Outline each blood parasite and name the species.
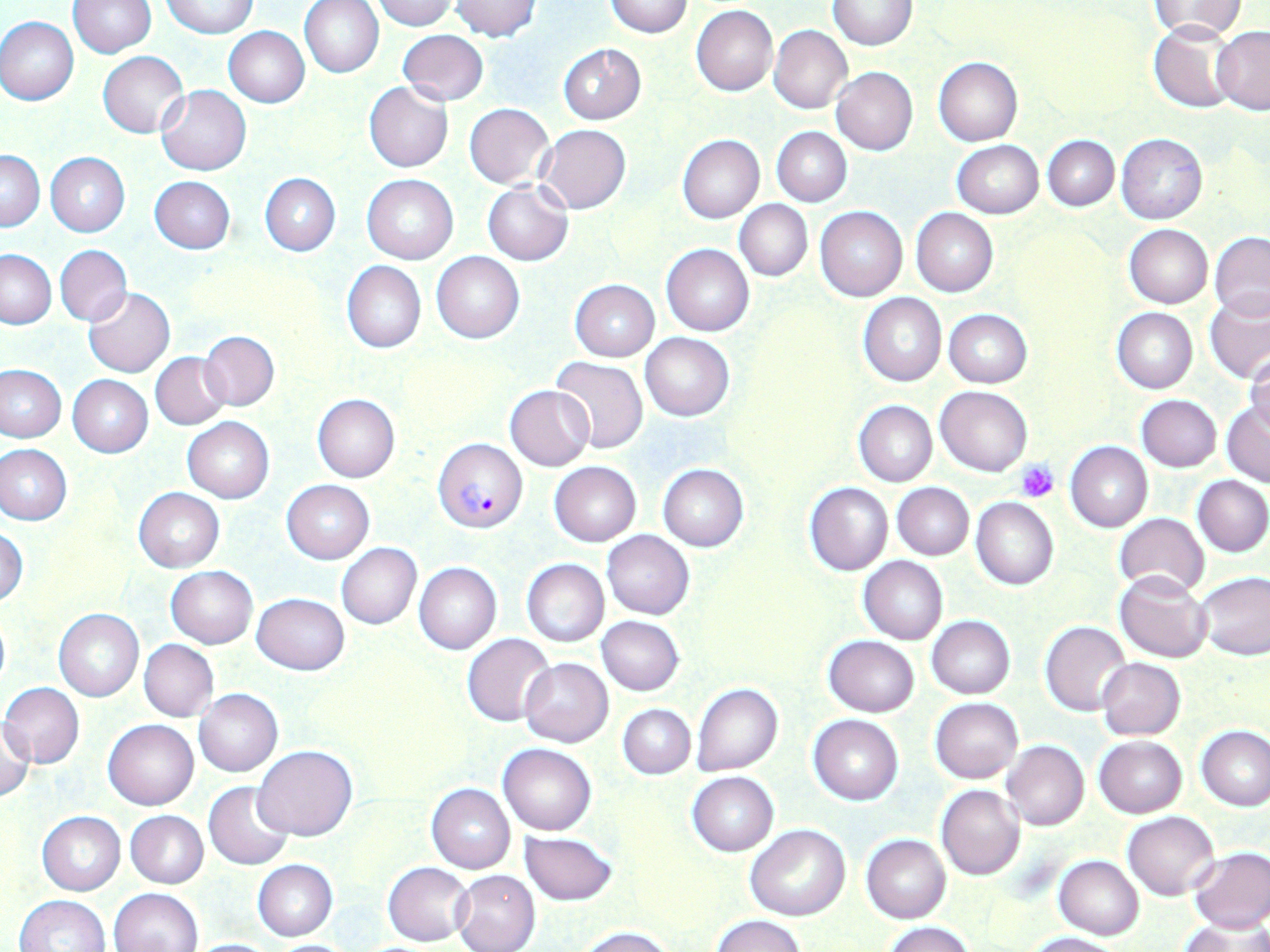
Approximate bounding boxes as named x1/y1/x2/y2 corners in pixels.
Plasmodium falciparum-infected red blood cells: (x1=434, y1=437, x2=527, y2=532).
No Plasmodium ovale, Plasmodium malariae, Plasmodium vivax, Babesia divergens, or Trypanosoma brucei observed.

Platelet locations: (x1=1014, y1=460, x2=1059, y2=502). Uninfected red blood cell locations: (x1=68, y1=0, x2=157, y2=58), (x1=299, y1=0, x2=385, y2=78), (x1=373, y1=0, x2=457, y2=30), (x1=448, y1=0, x2=542, y2=43), (x1=827, y1=0, x2=918, y2=50), (x1=1151, y1=0, x2=1249, y2=42), (x1=160, y1=1, x2=258, y2=37), (x1=605, y1=1, x2=693, y2=38), (x1=691, y1=5, x2=778, y2=96), (x1=1, y1=16, x2=79, y2=105), (x1=1148, y1=23, x2=1240, y2=112), (x1=769, y1=24, x2=852, y2=114), (x1=223, y1=26, x2=309, y2=107), (x1=1210, y1=26, x2=1270, y2=114), (x1=396, y1=30, x2=488, y2=106), (x1=558, y1=44, x2=647, y2=124), (x1=98, y1=52, x2=188, y2=137), (x1=933, y1=57, x2=1022, y2=145), (x1=831, y1=67, x2=918, y2=155), (x1=364, y1=82, x2=454, y2=172), (x1=157, y1=85, x2=250, y2=176), (x1=464, y1=103, x2=554, y2=189), (x1=536, y1=124, x2=631, y2=214), (x1=773, y1=127, x2=851, y2=206), (x1=1116, y1=133, x2=1208, y2=225), (x1=677, y1=134, x2=764, y2=223), (x1=1043, y1=135, x2=1119, y2=211), (x1=951, y1=141, x2=1042, y2=218), (x1=1, y1=149, x2=43, y2=231), (x1=46, y1=152, x2=130, y2=237), (x1=260, y1=173, x2=340, y2=255), (x1=361, y1=174, x2=457, y2=263), (x1=149, y1=176, x2=236, y2=254), (x1=483, y1=180, x2=573, y2=265), (x1=735, y1=201, x2=813, y2=281), (x1=815, y1=206, x2=907, y2=302), (x1=911, y1=207, x2=998, y2=296), (x1=1124, y1=224, x2=1213, y2=308), (x1=1210, y1=231, x2=1270, y2=320), (x1=54, y1=244, x2=132, y2=327), (x1=662, y1=244, x2=754, y2=336), (x1=0, y1=249, x2=55, y2=329), (x1=433, y1=252, x2=524, y2=343), (x1=341, y1=261, x2=426, y2=353), (x1=569, y1=279, x2=659, y2=360), (x1=84, y1=288, x2=175, y2=377), (x1=1204, y1=291, x2=1270, y2=382), (x1=858, y1=294, x2=946, y2=386), (x1=1112, y1=307, x2=1197, y2=393), (x1=944, y1=308, x2=1032, y2=387), (x1=198, y1=331, x2=279, y2=410), (x1=641, y1=332, x2=734, y2=421), (x1=398, y1=349, x2=488, y2=437), (x1=1245, y1=350, x2=1270, y2=435), (x1=150, y1=353, x2=230, y2=430), (x1=550, y1=357, x2=647, y2=455), (x1=0, y1=364, x2=68, y2=442), (x1=67, y1=375, x2=153, y2=457), (x1=506, y1=385, x2=594, y2=471), (x1=935, y1=386, x2=1032, y2=476), (x1=311, y1=394, x2=399, y2=482), (x1=1137, y1=395, x2=1221, y2=472), (x1=854, y1=400, x2=937, y2=487), (x1=1221, y1=402, x2=1270, y2=486), (x1=181, y1=417, x2=274, y2=503), (x1=1066, y1=441, x2=1152, y2=533), (x1=1, y1=444, x2=72, y2=525), (x1=549, y1=461, x2=642, y2=546), (x1=657, y1=464, x2=748, y2=552), (x1=1192, y1=475, x2=1270, y2=557), (x1=281, y1=480, x2=375, y2=563), (x1=892, y1=482, x2=974, y2=560), (x1=805, y1=483, x2=893, y2=574), (x1=134, y1=488, x2=223, y2=572), (x1=971, y1=497, x2=1058, y2=590), (x1=1114, y1=513, x2=1209, y2=596), (x1=0, y1=525, x2=27, y2=607), (x1=603, y1=530, x2=694, y2=619), (x1=336, y1=543, x2=421, y2=629), (x1=858, y1=557, x2=948, y2=644), (x1=521, y1=559, x2=608, y2=648), (x1=414, y1=562, x2=501, y2=654), (x1=166, y1=566, x2=257, y2=647), (x1=1115, y1=571, x2=1213, y2=662), (x1=1196, y1=571, x2=1270, y2=661), (x1=251, y1=593, x2=350, y2=674), (x1=54, y1=609, x2=143, y2=700), (x1=0, y1=611, x2=10, y2=692), (x1=596, y1=616, x2=684, y2=695), (x1=927, y1=616, x2=1015, y2=699), (x1=1040, y1=621, x2=1131, y2=715), (x1=463, y1=633, x2=554, y2=726), (x1=824, y1=635, x2=920, y2=717), (x1=140, y1=639, x2=218, y2=722), (x1=518, y1=657, x2=614, y2=747), (x1=1097, y1=658, x2=1185, y2=740), (x1=0, y1=682, x2=84, y2=768), (x1=692, y1=683, x2=783, y2=776), (x1=194, y1=689, x2=283, y2=776), (x1=930, y1=697, x2=1023, y2=783), (x1=618, y1=704, x2=695, y2=779), (x1=807, y1=714, x2=903, y2=804), (x1=0, y1=718, x2=35, y2=802), (x1=104, y1=719, x2=199, y2=810), (x1=1196, y1=726, x2=1269, y2=812), (x1=1094, y1=736, x2=1186, y2=818), (x1=1001, y1=740, x2=1089, y2=831), (x1=499, y1=743, x2=595, y2=834), (x1=253, y1=745, x2=357, y2=841), (x1=688, y1=772, x2=777, y2=856), (x1=204, y1=781, x2=295, y2=869), (x1=426, y1=784, x2=516, y2=874), (x1=936, y1=785, x2=1025, y2=880), (x1=126, y1=810, x2=208, y2=888), (x1=38, y1=811, x2=126, y2=895), (x1=1123, y1=811, x2=1219, y2=901), (x1=746, y1=824, x2=850, y2=921), (x1=521, y1=831, x2=616, y2=906), (x1=862, y1=835, x2=951, y2=923), (x1=1188, y1=847, x2=1270, y2=932), (x1=1054, y1=855, x2=1144, y2=939), (x1=253, y1=859, x2=338, y2=940), (x1=382, y1=862, x2=473, y2=946), (x1=452, y1=869, x2=540, y2=952), (x1=109, y1=888, x2=201, y2=952), (x1=13, y1=894, x2=109, y2=952), (x1=712, y1=915, x2=806, y2=952), (x1=1182, y1=919, x2=1267, y2=951), (x1=883, y1=922, x2=976, y2=952), (x1=578, y1=926, x2=676, y2=952), (x1=1024, y1=932, x2=1123, y2=952), (x1=184, y1=938, x2=281, y2=951), (x1=266, y1=939, x2=363, y2=951). Slide-level diagnosis: Plasmodium falciparum. One field of a larger specimen. Thin blood film. May-Grünwald-Giemsa stain. Captured at 1000x magnification. Image is 1270×952 pixels. Light microscopy.